Identify the blood parasite species.
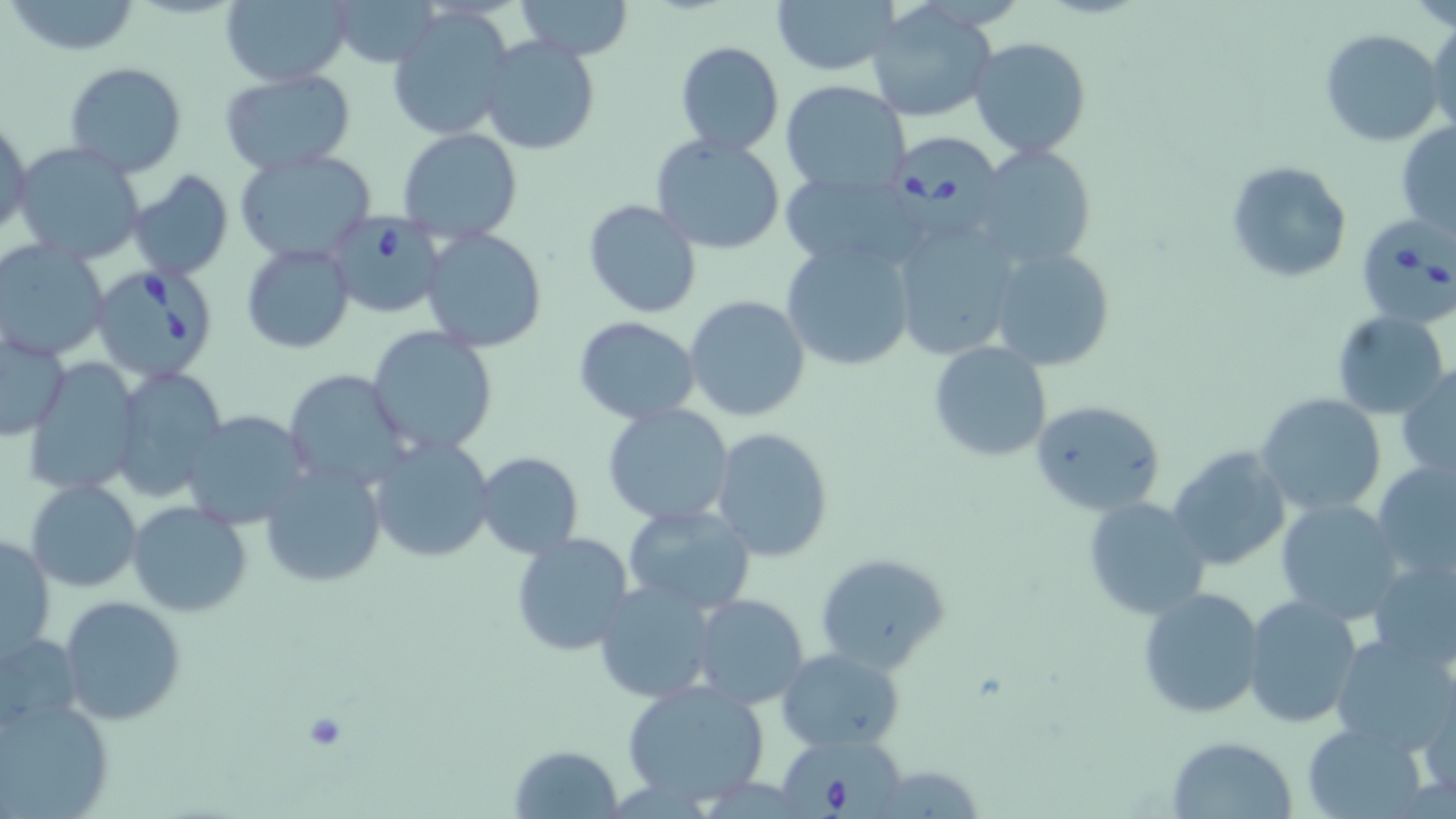
Babesia divergens.

Approximate bounding boxes as [x1, y1, x2, y2] in pixels. Platelet locations: [301, 712, 350, 753]. Babesia divergens-infected red blood cell locations: [889, 131, 1006, 239], [324, 211, 446, 318], [1356, 217, 1456, 329], [88, 263, 223, 382], [780, 731, 907, 819]. Uninfected red blood cell locations: [219, 0, 351, 87], [331, 0, 437, 67], [514, 0, 635, 61], [770, 0, 900, 76], [1405, 0, 1456, 29], [7, 1, 143, 55], [867, 5, 996, 125], [389, 10, 514, 139], [1427, 19, 1456, 135], [1319, 29, 1444, 147], [968, 36, 1093, 157], [479, 37, 600, 156], [673, 40, 785, 157], [64, 61, 188, 177], [218, 72, 356, 177], [778, 80, 913, 199], [1, 120, 32, 240], [1396, 121, 1456, 237], [396, 128, 522, 243], [649, 133, 788, 256], [12, 141, 149, 265], [967, 142, 1100, 273], [233, 149, 379, 264], [1226, 160, 1352, 282], [780, 168, 931, 269], [125, 169, 234, 281], [582, 199, 702, 319], [890, 216, 1025, 361], [421, 228, 548, 351], [0, 239, 109, 362], [780, 241, 916, 373], [241, 242, 354, 353], [986, 246, 1115, 371], [685, 296, 812, 423], [1331, 310, 1449, 418], [572, 317, 701, 425], [366, 326, 497, 455], [1, 328, 71, 443], [928, 342, 1052, 461], [23, 359, 141, 494], [1398, 362, 1456, 480], [112, 367, 229, 502], [281, 368, 412, 491], [1256, 392, 1388, 518], [1029, 398, 1168, 517], [603, 403, 735, 528], [179, 411, 309, 529], [712, 427, 834, 562], [369, 437, 495, 562], [1166, 445, 1291, 572], [472, 452, 584, 560], [1371, 458, 1456, 589], [259, 463, 386, 589], [25, 479, 142, 591], [1083, 495, 1212, 620], [1274, 498, 1404, 623], [127, 502, 254, 618], [622, 505, 756, 614], [510, 531, 636, 659], [1, 532, 55, 662], [814, 551, 952, 673], [1366, 556, 1456, 671], [594, 578, 717, 704], [1136, 586, 1266, 721], [691, 594, 811, 710], [1243, 594, 1363, 730], [57, 596, 186, 725], [0, 632, 83, 732], [1331, 634, 1456, 753], [776, 648, 906, 749], [620, 680, 773, 806], [1417, 688, 1455, 807], [0, 694, 112, 818], [1302, 720, 1430, 818], [1165, 737, 1299, 819], [509, 743, 625, 819]. May-Grünwald-Giemsa-stained preparation. Image is 1456×819 pixels. Captured at 1000x magnification. Light microscopy. Single field of view. Thin blood smear.